Report the malaria status of this cell.
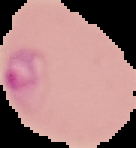

Parasitized.

Cell region segmented out of the field of view; the surrounding area is masked to black. From a thin blood film. Image is 136×148 pixels.